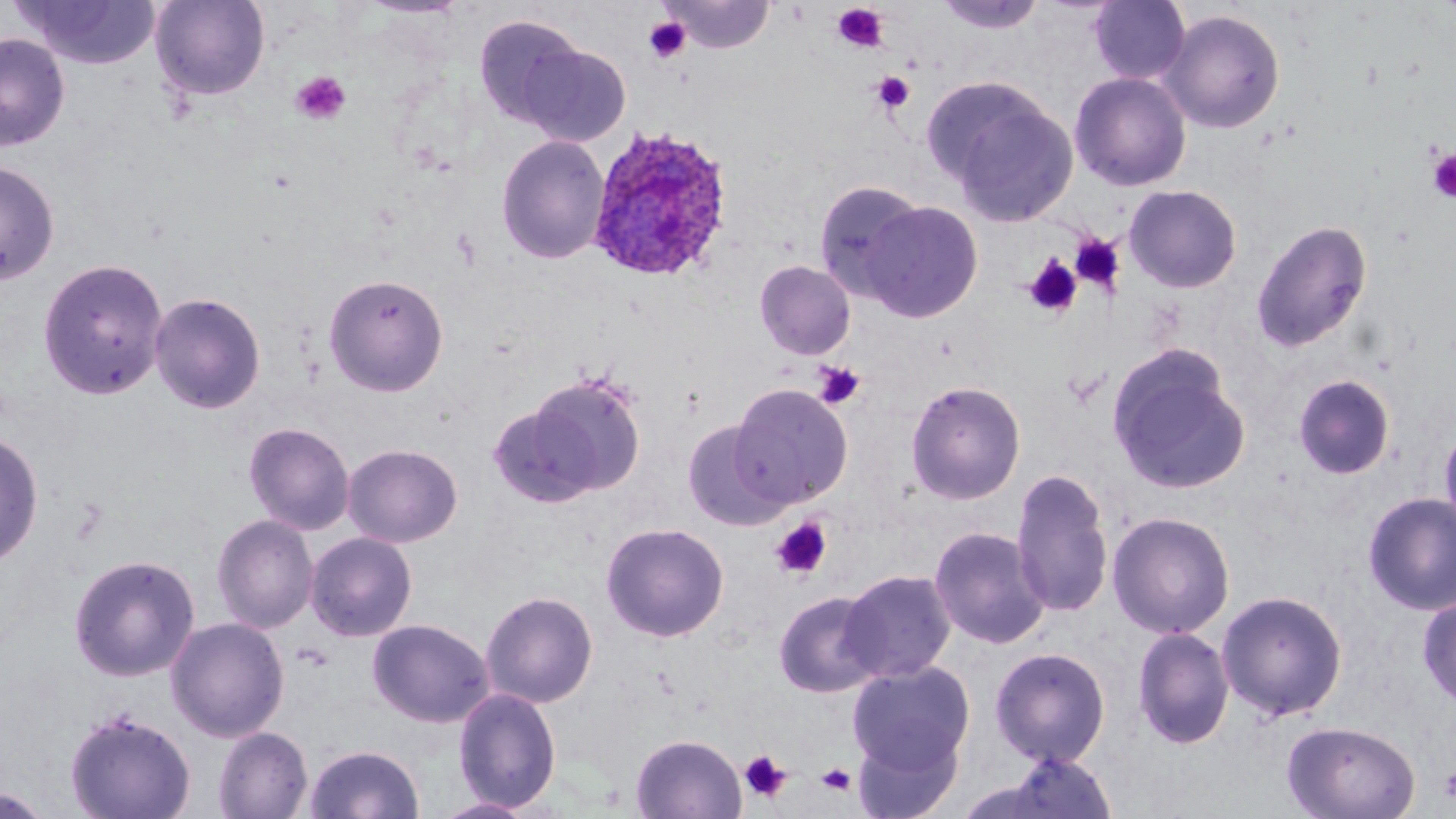

Approximate bounding boxes as (x1,y1)-(x2,y2) corner pairs in pixels. Uninfected red blood cell locations: (14,0)-(161,69), (150,0)-(271,101), (660,0)-(776,53), (934,0)-(1047,34), (1088,0)-(1191,85), (1159,9)-(1285,134), (473,14)-(587,126), (0,33)-(70,151), (518,44)-(631,146), (1070,71)-(1192,191), (937,85)-(1078,227), (496,134)-(610,264), (0,160)-(59,285), (813,180)-(926,300), (1123,184)-(1242,293), (862,200)-(984,323), (1251,219)-(1373,352), (38,257)-(169,399), (754,260)-(856,360), (323,272)-(449,396), (149,291)-(266,414), (1107,345)-(1250,496), (524,371)-(647,498), (1292,374)-(1395,480), (906,379)-(1026,505), (729,383)-(853,509), (681,419)-(791,530), (243,421)-(355,535), (1439,421)-(1456,538), (0,431)-(44,568), (342,443)-(463,547), (1011,467)-(1115,617), (1362,492)-(1456,616), (1107,511)-(1235,638), (212,514)-(319,634), (601,521)-(730,642), (929,525)-(1050,649), (305,531)-(418,642), (68,553)-(200,682), (839,570)-(956,683), (1216,589)-(1348,721), (481,590)-(598,708), (773,591)-(885,697), (1417,593)-(1456,709), (165,616)-(290,742), (367,618)-(495,728), (1132,626)-(1235,749), (990,646)-(1110,766), (847,661)-(975,774), (452,686)-(561,812), (64,707)-(196,819), (1282,720)-(1421,819), (214,726)-(313,819), (853,730)-(962,818), (631,733)-(746,818), (304,743)-(425,819), (1002,751)-(1118,819), (1,786)-(54,819), (431,797)-(537,818). Platelet locations: (831,3)-(889,53), (644,17)-(690,62), (290,70)-(351,125), (872,71)-(914,113), (1427,149)-(1456,203), (1070,233)-(1126,294), (1023,255)-(1084,318), (813,362)-(865,409), (771,518)-(832,579), (739,749)-(792,803), (816,763)-(857,795), (1440,769)-(1456,802). Plasmodium ovale-infected red blood cell locations: (585,126)-(734,283). Slide-level diagnosis: Plasmodium ovale. Light microscopy. Image is 1456×819 pixels. One field of a larger specimen. 1000x magnification. May-Grünwald-Giemsa stain. Thin blood smear.